Assess for Plasmodium parasites.
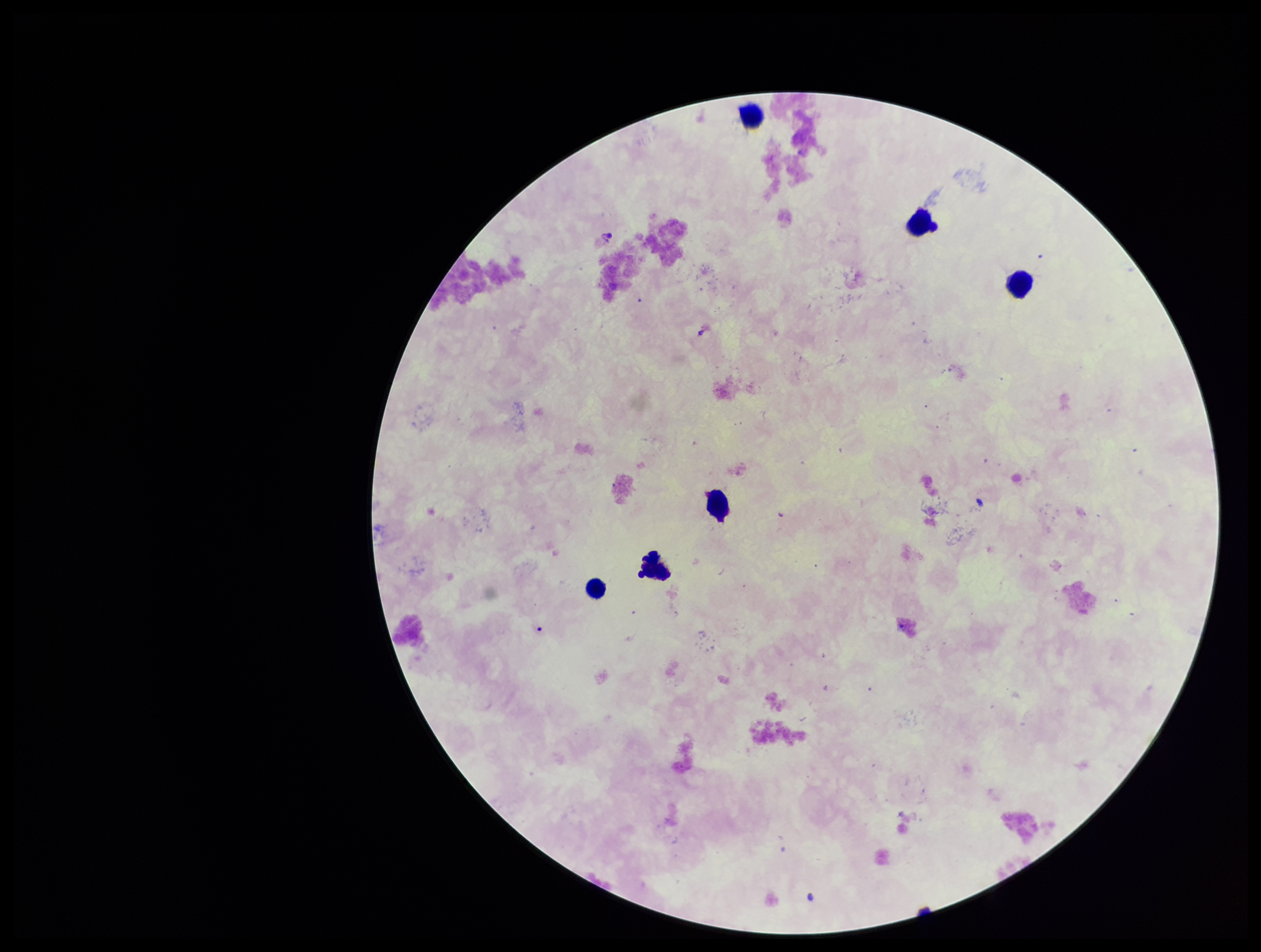
None identified.

preparation = thick
parasite count = 0
field of view = single
leukocyte count = 6
capture = smartphone photograph through the microscope eyepiece
patient malaria status = negative
stain = Giemsa
image size = 1261×952 pixels